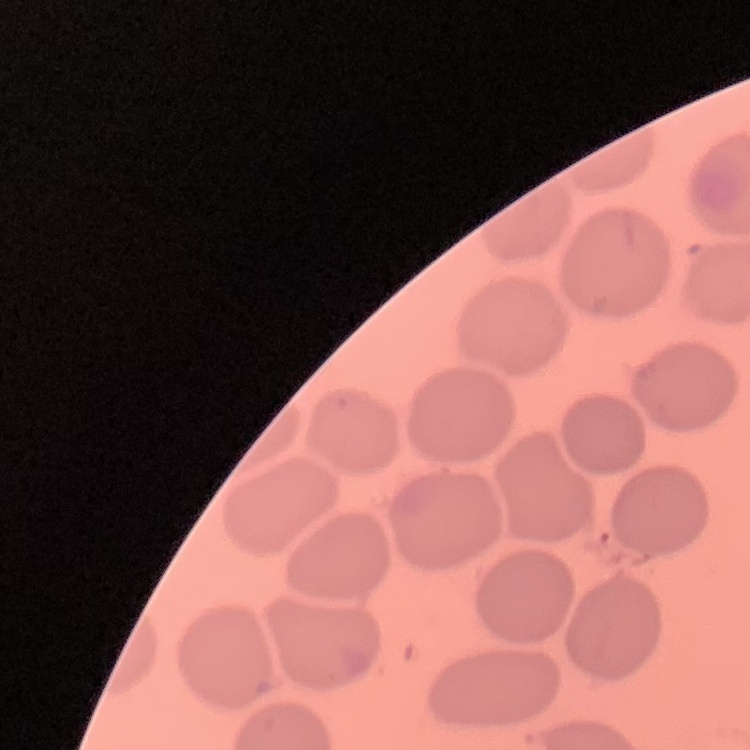
red_blood_cell_morphology: no rouleaux formation
image_type: one tile cut from a larger photomicrograph
preparation: thin blood smear
stain: Field's or Giemsa